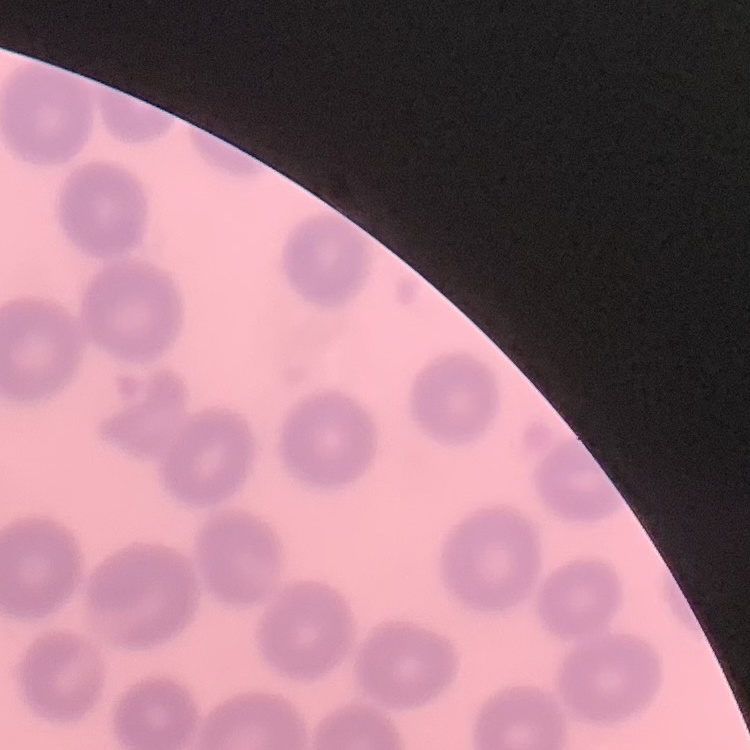

The erythrocytes show no rouleaux formation. Square crop of a larger photomicrograph. Thin blood film. Stained with either Field's or Giemsa.